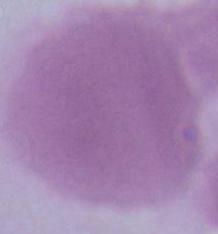
modality = photomicrograph
identification = red blood cell
magnification = 1000x